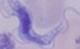

Summary:
  - Identification: trypanosome
  - Modality: micrograph
  - Magnification: 1000x